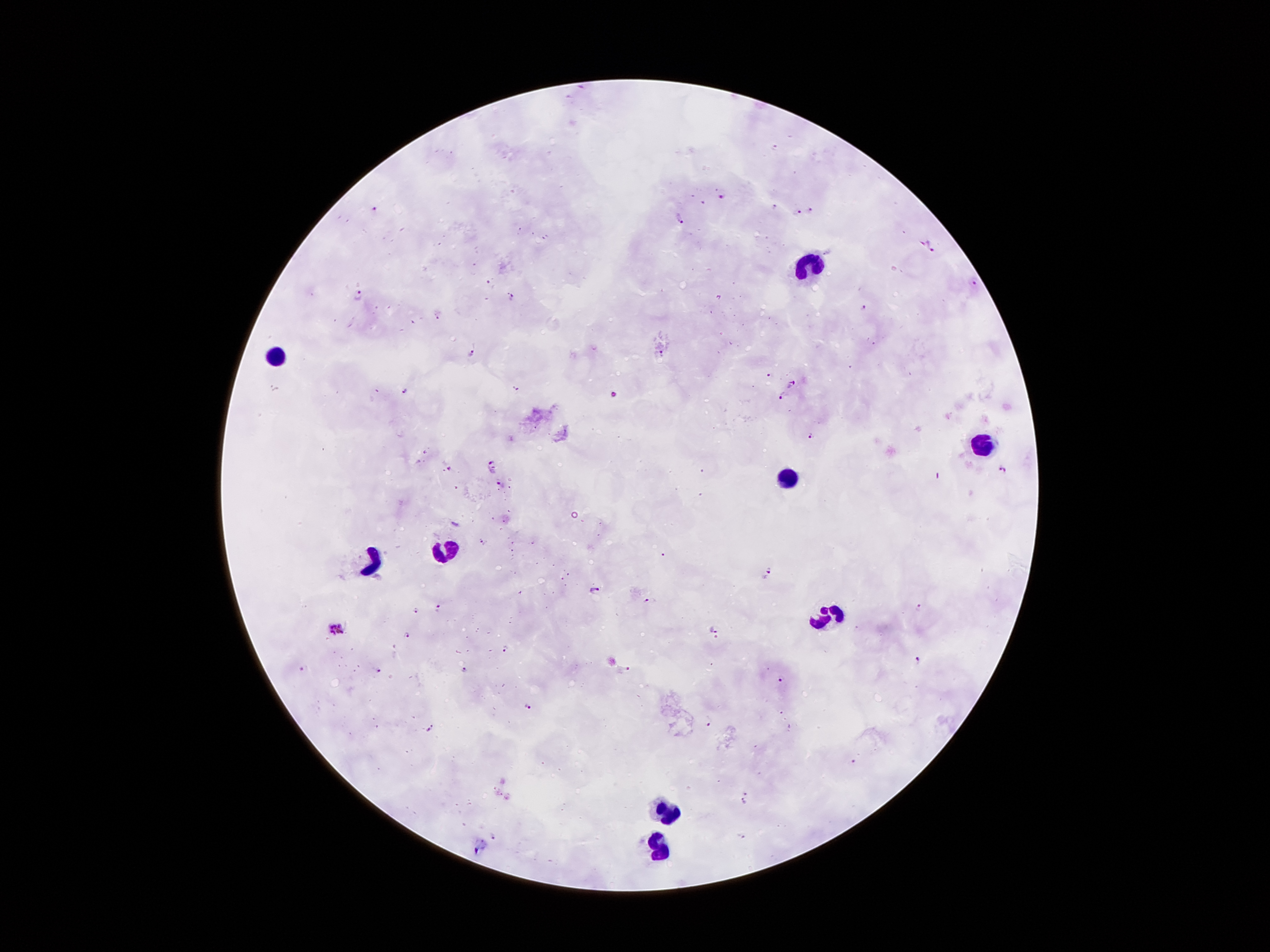

Approximate centers as [x, y] in pixels.
Summary:
  - Malaria parasite locations: [720, 197], [375, 206], [774, 209], [811, 211], [797, 213], [683, 216], [931, 247], [491, 281], [974, 284], [357, 295], [511, 297], [867, 306], [659, 352], [472, 354], [767, 374], [792, 384], [517, 386], [406, 389], [615, 393], [781, 395], [811, 435], [490, 463], [450, 469], [1004, 470], [502, 485], [482, 541], [663, 555], [769, 572], [593, 588], [651, 601], [919, 606], [436, 609], [413, 610], [336, 625], [711, 627], [404, 632], [506, 648], [919, 661], [300, 667], [628, 668], [379, 670], [463, 670], [783, 682], [525, 707], [710, 723], [431, 727], [854, 762], [747, 791], [743, 800], [742, 836], [494, 837]
  - Leukocyte locations: [809, 259], [278, 359], [979, 448], [793, 477], [444, 552], [375, 566], [823, 616], [666, 815], [659, 844]
  - Magnification: 100x
  - Preparation: thick blood smear
  - Stain: Giemsa
  - Capture: smartphone camera through the microscope eyepiece
  - Image size: 1270×952 pixels
  - Patient malaria status: positive for Plasmodium falciparum
  - Field of view: one from this slide